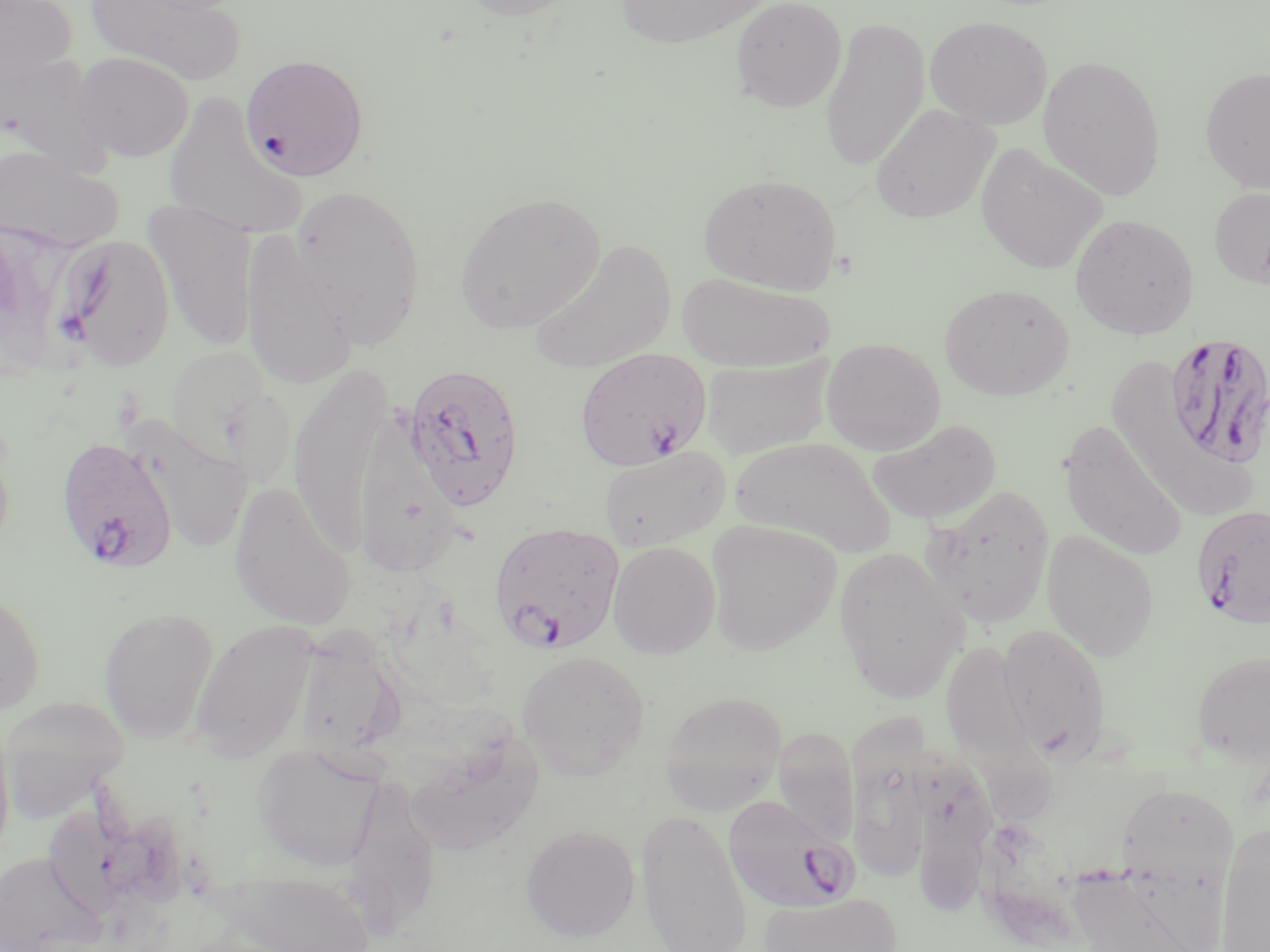
Approximate bounding boxes as named x1/y1/x2/y2 corners in pixels. Plasmodium falciparum-infected red blood cell locations: (x1=1163, y1=332, x2=1270, y2=470), (x1=575, y1=347, x2=712, y2=470), (x1=402, y1=363, x2=525, y2=511), (x1=55, y1=435, x2=178, y2=573), (x1=1190, y1=504, x2=1270, y2=631), (x1=489, y1=522, x2=626, y2=655), (x1=721, y1=793, x2=860, y2=916). Uninfected red blood cell locations: (x1=0, y1=0, x2=78, y2=87), (x1=86, y1=0, x2=245, y2=84), (x1=457, y1=0, x2=583, y2=21), (x1=615, y1=0, x2=768, y2=49), (x1=730, y1=0, x2=847, y2=112), (x1=925, y1=15, x2=1053, y2=129), (x1=820, y1=18, x2=930, y2=171), (x1=0, y1=51, x2=108, y2=168), (x1=72, y1=51, x2=194, y2=161), (x1=240, y1=53, x2=370, y2=181), (x1=1037, y1=54, x2=1167, y2=200), (x1=1200, y1=66, x2=1270, y2=193), (x1=163, y1=92, x2=307, y2=240), (x1=871, y1=104, x2=998, y2=223), (x1=975, y1=143, x2=1108, y2=274), (x1=1, y1=146, x2=125, y2=253), (x1=698, y1=173, x2=842, y2=295), (x1=291, y1=184, x2=427, y2=346), (x1=1209, y1=186, x2=1270, y2=288), (x1=453, y1=190, x2=606, y2=334), (x1=144, y1=200, x2=260, y2=351), (x1=1069, y1=212, x2=1199, y2=339), (x1=0, y1=218, x2=57, y2=370), (x1=240, y1=230, x2=357, y2=391), (x1=55, y1=233, x2=175, y2=371), (x1=530, y1=238, x2=676, y2=375), (x1=676, y1=271, x2=834, y2=373), (x1=939, y1=282, x2=1075, y2=401), (x1=821, y1=337, x2=945, y2=454), (x1=163, y1=344, x2=281, y2=471), (x1=699, y1=353, x2=834, y2=458), (x1=1115, y1=363, x2=1249, y2=509), (x1=288, y1=367, x2=391, y2=556), (x1=357, y1=396, x2=460, y2=576), (x1=868, y1=418, x2=1002, y2=526), (x1=132, y1=421, x2=253, y2=555), (x1=1058, y1=421, x2=1189, y2=563), (x1=730, y1=437, x2=897, y2=558), (x1=598, y1=446, x2=732, y2=552), (x1=229, y1=480, x2=356, y2=631), (x1=921, y1=484, x2=1055, y2=628), (x1=704, y1=520, x2=841, y2=655), (x1=1041, y1=530, x2=1159, y2=661), (x1=608, y1=541, x2=721, y2=658), (x1=834, y1=546, x2=967, y2=704), (x1=0, y1=584, x2=45, y2=716), (x1=98, y1=606, x2=219, y2=743), (x1=189, y1=619, x2=321, y2=762), (x1=996, y1=622, x2=1111, y2=761), (x1=292, y1=625, x2=406, y2=760), (x1=938, y1=645, x2=1053, y2=822), (x1=1191, y1=648, x2=1270, y2=765), (x1=516, y1=650, x2=650, y2=779), (x1=660, y1=690, x2=787, y2=814), (x1=0, y1=695, x2=131, y2=818), (x1=0, y1=713, x2=16, y2=863), (x1=773, y1=727, x2=860, y2=846), (x1=405, y1=732, x2=543, y2=858), (x1=848, y1=733, x2=930, y2=885), (x1=252, y1=742, x2=383, y2=872), (x1=913, y1=744, x2=994, y2=914), (x1=344, y1=777, x2=441, y2=936), (x1=1120, y1=781, x2=1244, y2=952), (x1=41, y1=804, x2=163, y2=918), (x1=636, y1=810, x2=753, y2=952), (x1=1216, y1=821, x2=1270, y2=952), (x1=521, y1=824, x2=640, y2=941), (x1=1, y1=850, x2=104, y2=952), (x1=1064, y1=864, x2=1217, y2=952), (x1=208, y1=872, x2=379, y2=952), (x1=759, y1=892, x2=903, y2=952). Slide-level diagnosis: Plasmodium falciparum. One field of a larger specimen. 1000x magnification. Light microscopy. May-Grünwald-Giemsa stain. Thin blood film. Image is 1270×952 pixels.